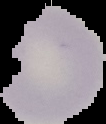
Summary:
  - Image size: 106×124 pixels
  - Preparation: thin blood film
  - Malaria status: uninfected
  - Image type: segmented cell region on a black background